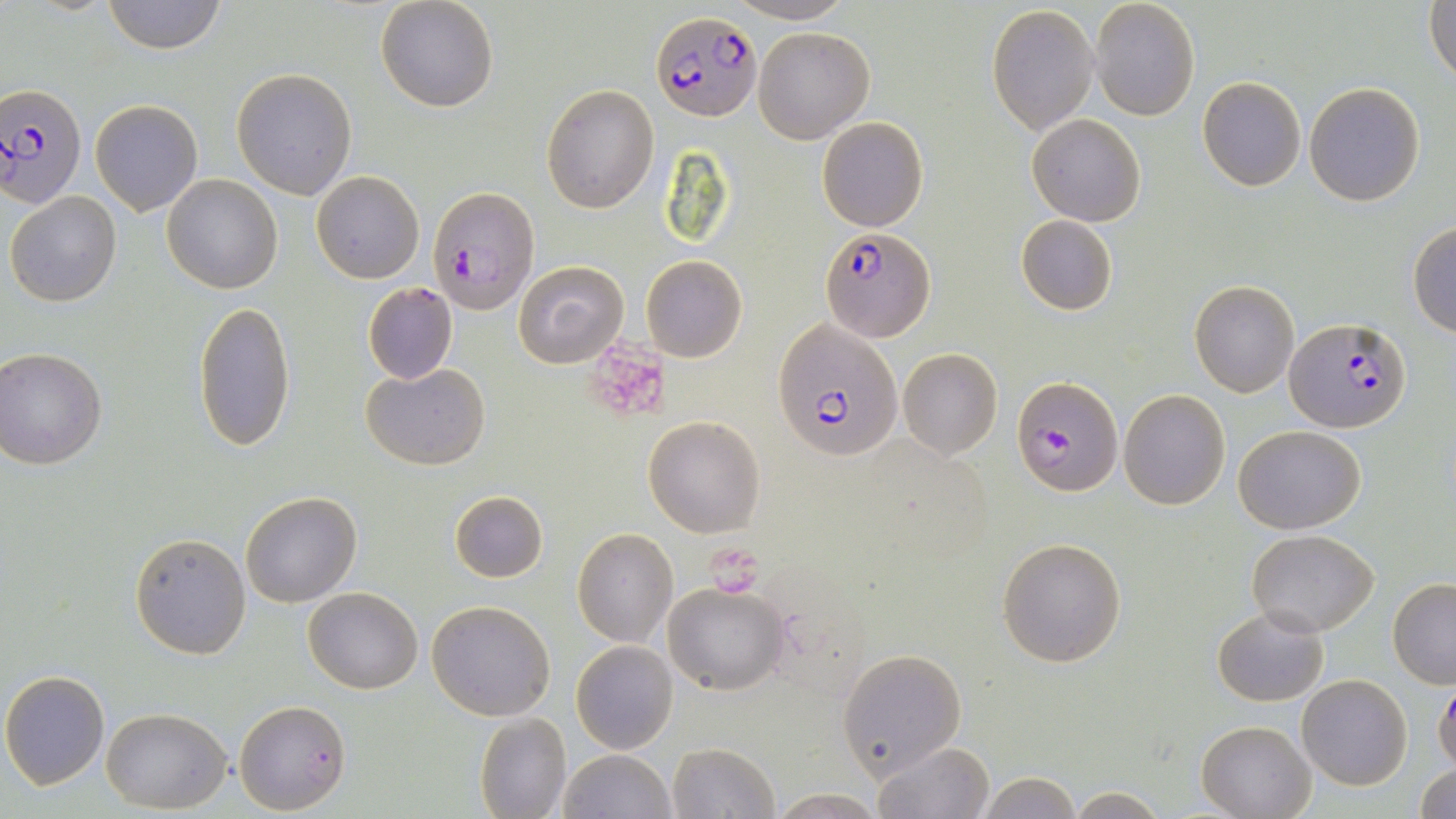

Summary:
  - Coordinate format: approximate bounding boxes as [x1, y1, x2, y2] in pixels
  - Platelet locations: [587, 341, 672, 415], [706, 545, 764, 599]
  - Plasmodium falciparum-infected red blood cell locations: [650, 11, 761, 120], [0, 85, 88, 207], [427, 186, 539, 313], [819, 227, 937, 344], [1285, 317, 1412, 433], [774, 320, 904, 461], [1013, 376, 1122, 495]
  - Uninfected red blood cell locations: [101, 0, 227, 54], [726, 0, 858, 24], [1090, 0, 1200, 121], [1425, 0, 1456, 87], [375, 1, 500, 113], [987, 4, 1101, 135], [754, 26, 874, 143], [231, 69, 357, 199], [1197, 77, 1305, 191], [1303, 82, 1426, 207], [540, 83, 660, 213], [91, 99, 203, 216], [1026, 113, 1146, 226], [816, 116, 928, 231], [311, 171, 425, 284], [163, 174, 283, 294], [6, 191, 122, 307], [1015, 215, 1118, 316], [1408, 222, 1455, 337], [641, 254, 748, 363], [512, 259, 628, 367], [1189, 280, 1301, 399], [362, 283, 458, 384], [193, 300, 297, 451], [897, 348, 1004, 461], [0, 349, 107, 468], [361, 361, 490, 469], [1118, 389, 1231, 511], [643, 416, 765, 537], [1233, 425, 1365, 532], [447, 490, 548, 584], [240, 491, 361, 607], [572, 528, 678, 647], [1247, 529, 1380, 638], [130, 532, 250, 658], [997, 536, 1127, 669], [1387, 578, 1456, 688], [663, 582, 788, 695], [303, 586, 423, 694], [426, 599, 557, 721], [1211, 605, 1328, 707], [571, 640, 679, 753], [837, 647, 968, 781], [1, 670, 112, 790], [1297, 674, 1412, 789], [1433, 678, 1456, 772], [234, 700, 351, 814], [101, 707, 231, 812], [474, 713, 571, 819], [1196, 719, 1314, 819], [871, 740, 995, 818], [666, 743, 779, 819], [555, 750, 676, 819], [1413, 763, 1456, 818], [975, 772, 1083, 818], [1065, 788, 1171, 818], [766, 791, 887, 818]
  - Slide-level diagnosis: Plasmodium falciparum
  - Field of view: single
  - Modality: optical microscopy
  - Preparation: thin blood smear
  - Image size: 1456×819 pixels
  - Magnification: 1000x
  - Stain: May-Grünwald-Giemsa